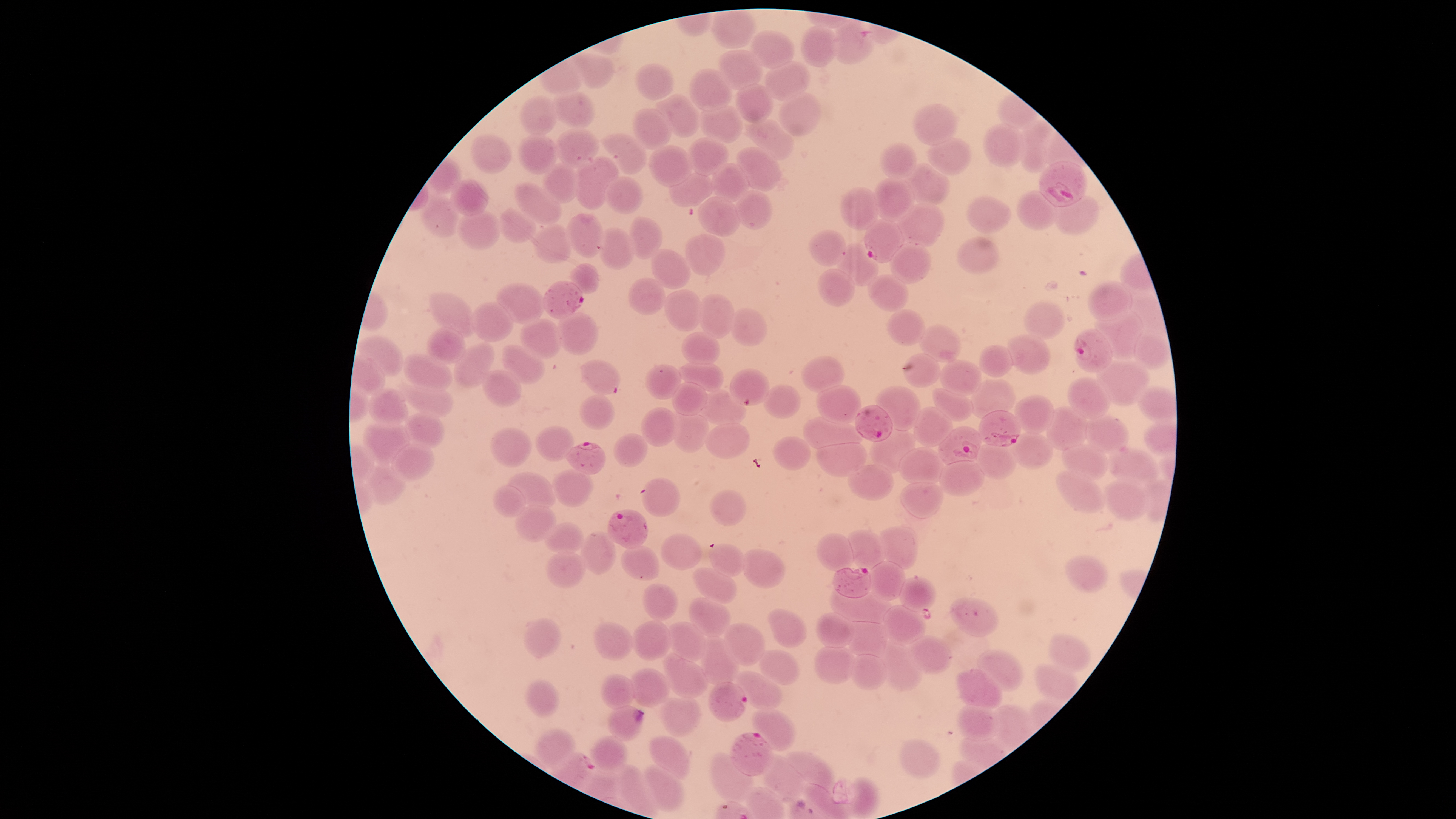

Approximate bounding boxes as (left, top, right, bottom) in pixels.
Summary:
  - Uninfected red blood cells: (800, 26, 839, 67), (751, 30, 794, 68), (718, 49, 761, 90), (572, 54, 614, 89), (764, 60, 810, 101), (636, 63, 673, 100), (689, 69, 732, 111), (737, 83, 774, 123), (551, 91, 596, 128), (778, 92, 820, 136), (655, 95, 702, 137), (521, 96, 559, 135), (700, 103, 743, 143), (912, 103, 956, 146), (632, 109, 672, 149), (743, 119, 794, 160), (1019, 120, 1052, 173), (983, 124, 1023, 168), (557, 129, 599, 168), (516, 133, 560, 174), (472, 134, 511, 172), (602, 134, 647, 174), (688, 137, 729, 175), (927, 139, 971, 175), (880, 143, 916, 179), (649, 145, 692, 187), (736, 147, 780, 192), (573, 157, 619, 210), (543, 163, 579, 203), (710, 163, 749, 202), (905, 163, 951, 207), (668, 173, 713, 208), (604, 177, 643, 214), (873, 177, 915, 222), (449, 179, 490, 215), (515, 183, 562, 223), (840, 187, 879, 231), (735, 189, 772, 229), (1014, 191, 1058, 230), (1055, 196, 1098, 234), (420, 197, 458, 237), (700, 197, 738, 236), (967, 197, 1012, 233), (898, 202, 945, 246), (499, 208, 536, 243), (458, 210, 502, 249), (565, 214, 603, 258), (629, 217, 661, 260), (534, 221, 571, 263), (599, 228, 635, 271), (809, 229, 845, 266), (684, 234, 725, 276), (958, 237, 999, 274), (836, 243, 878, 287), (889, 243, 931, 285), (650, 249, 691, 289), (570, 264, 598, 295), (817, 269, 856, 307), (868, 275, 909, 312), (629, 278, 665, 315), (1087, 282, 1133, 322), (497, 284, 544, 324), (664, 290, 703, 331), (428, 293, 474, 337), (700, 294, 734, 339), (1023, 300, 1066, 339), (472, 302, 513, 342), (728, 308, 768, 345), (886, 309, 925, 347), (1095, 311, 1144, 360), (557, 312, 597, 355), (519, 319, 562, 358), (919, 325, 961, 362), (426, 327, 467, 363), (1134, 328, 1171, 369), (682, 332, 720, 364), (1008, 335, 1051, 374), (358, 336, 402, 377), (453, 343, 495, 389), (502, 344, 545, 385), (980, 345, 1013, 377), (904, 352, 940, 388), (404, 354, 453, 389), (802, 357, 844, 392), (1097, 359, 1151, 406), (580, 360, 620, 395), (940, 360, 983, 397), (681, 363, 723, 391), (646, 365, 681, 400), (482, 370, 521, 406), (1068, 377, 1110, 419), (971, 380, 1015, 419), (398, 381, 453, 417), (672, 382, 706, 416), (764, 385, 801, 418), (816, 385, 861, 424), (876, 387, 920, 431), (1138, 387, 1177, 422), (369, 389, 408, 429), (697, 389, 746, 427), (932, 389, 974, 422), (579, 394, 615, 431), (1013, 394, 1053, 435), (1045, 406, 1088, 451), (641, 407, 679, 447), (912, 408, 954, 448), (402, 413, 444, 448), (671, 413, 709, 453), (804, 415, 864, 448), (1085, 416, 1129, 455), (705, 423, 749, 459), (362, 424, 410, 463), (535, 426, 574, 462), (489, 428, 530, 467), (869, 429, 917, 473), (1010, 432, 1054, 470), (614, 433, 647, 468), (773, 435, 811, 471), (816, 443, 867, 477), (391, 445, 434, 482), (977, 445, 1017, 479), (1062, 445, 1108, 480), (899, 447, 945, 484), (1108, 449, 1159, 485), (940, 460, 985, 497), (849, 464, 893, 500), (366, 466, 404, 503), (551, 469, 594, 508), (1056, 469, 1106, 514), (507, 472, 555, 507), (642, 478, 681, 517), (1104, 478, 1151, 520), (900, 482, 944, 520), (492, 484, 525, 517), (710, 490, 746, 526), (515, 505, 556, 542), (545, 523, 583, 554), (880, 528, 916, 570), (848, 531, 886, 570), (579, 532, 618, 573), (659, 533, 701, 570), (816, 533, 854, 572), (708, 544, 744, 576), (620, 547, 661, 581), (742, 548, 784, 587), (546, 553, 585, 589), (1066, 554, 1108, 592), (868, 561, 905, 600), (693, 568, 736, 605), (900, 576, 936, 612), (642, 583, 679, 620), (830, 589, 891, 624), (689, 598, 731, 637), (950, 598, 999, 637), (882, 605, 925, 645), (768, 608, 808, 647), (817, 613, 854, 648), (523, 618, 560, 658), (632, 620, 671, 661), (842, 621, 888, 657), (593, 622, 632, 662), (669, 622, 705, 662), (725, 622, 765, 667), (909, 635, 951, 673), (697, 636, 739, 686), (1049, 636, 1089, 671), (880, 640, 922, 692), (813, 647, 855, 683), (759, 650, 801, 684), (977, 650, 1023, 692), (664, 653, 707, 699), (850, 655, 887, 690), (1034, 664, 1079, 703), (630, 669, 670, 708), (956, 670, 1001, 709), (735, 671, 783, 711), (600, 674, 635, 709), (526, 680, 559, 717), (660, 697, 701, 737), (956, 704, 999, 741), (608, 706, 643, 741), (751, 710, 795, 750), (536, 729, 575, 768), (648, 735, 692, 780), (589, 736, 628, 774), (899, 739, 939, 779), (786, 750, 835, 789), (709, 753, 753, 802), (759, 753, 803, 801), (644, 764, 684, 811), (617, 765, 658, 818)
  - Parasitized red blood cells: (832, 20, 875, 65), (1039, 162, 1088, 207), (864, 220, 905, 263), (543, 281, 584, 319), (1074, 329, 1113, 373), (730, 369, 769, 406), (854, 405, 892, 442), (979, 411, 1021, 446), (939, 427, 981, 465), (565, 441, 606, 474), (607, 509, 649, 549), (832, 567, 872, 599), (708, 682, 748, 722), (730, 732, 772, 776)
  - Preparation: thin blood smear
  - Capture: smartphone photograph through the microscope eyepiece
  - Presence: malaria parasites identified
  - Stain: Giemsa
  - Image size: 1456×819 pixels
  - Field of view: single
  - Visible region: circular
  - Species: Plasmodium falciparum